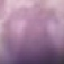

Result: negative for malaria parasites. Cell patch, automatically extracted from a larger field of view and resized to 64 × 64 pixels. Thin blood smear. Photographed with a smartphone camera at the microscope eyepiece. Giemsa-stained preparation.